Identify the parasite.
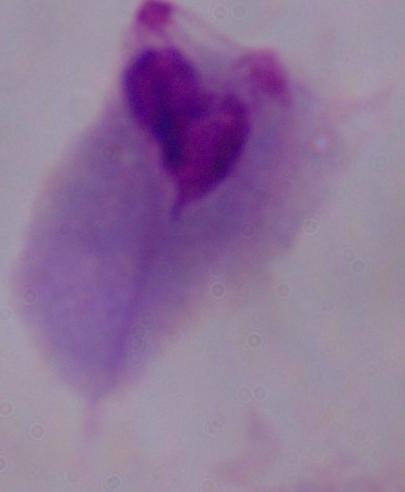
A trichomonad.

Summary:
  - Magnification: 1000x
  - Modality: photomicrograph